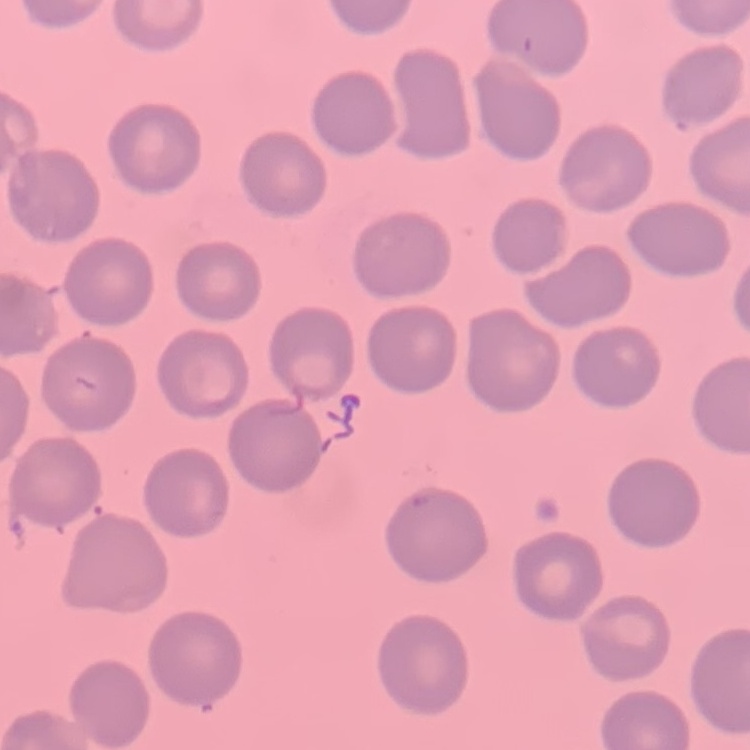
red blood cell morphology = no rouleaux formation
preparation = thin blood smear
image type = one tile cut from a larger photomicrograph
stain = Field's or Giemsa